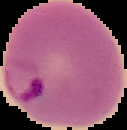
preparation = thin blood film
result = malaria parasites detected
image size = 127×130 pixels
image type = segmented cell region on a black background